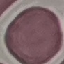
{
  "malaria_status": "uninfected",
  "capture": "smartphone through the microscope eyepiece",
  "stain": "Giemsa",
  "preparation": "thin blood film",
  "image_type": "cell patch, automatically extracted from a larger field of view and resized to 64 × 64 pixels"
}